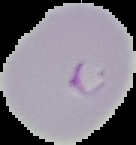 Malaria status: parasitized. Segmented cell region on a black background. Image is 136×145 pixels. From a thin blood film.